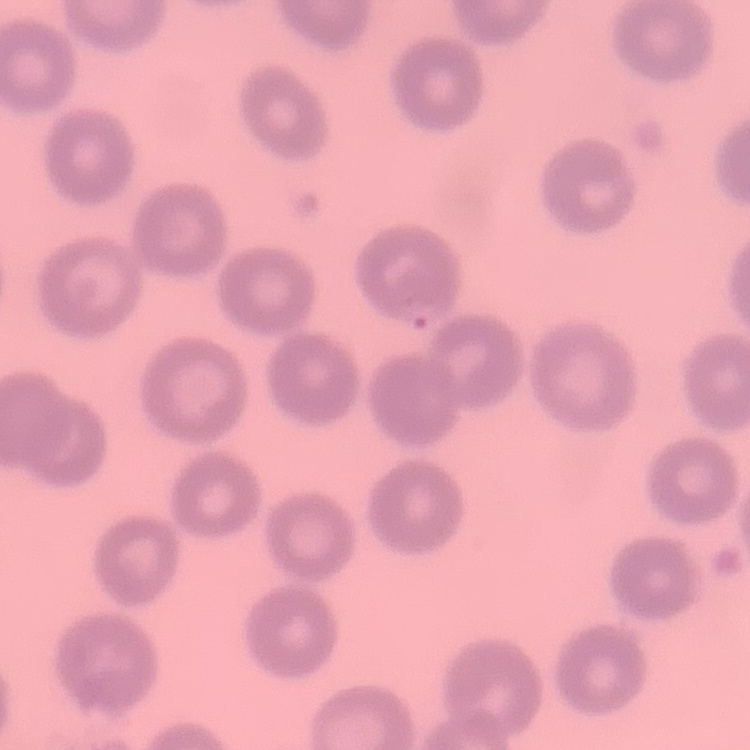
Summary:
  - Erythrocyte morphology: no rouleaux formation
  - Image type: square crop of a larger photomicrograph
  - Stain: Field's or Giemsa
  - Preparation: thin blood smear